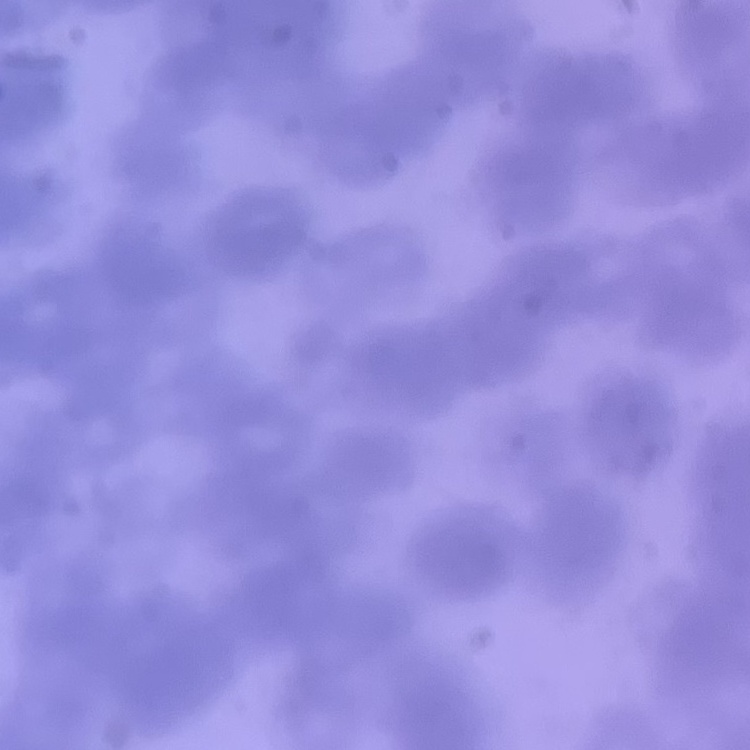

Summary:
  - Erythrocyte morphology: rouleaux formation
  - Image type: square crop of a larger photomicrograph
  - Preparation: thin blood smear
  - Stain: Field's or Giemsa